Identify the blood parasite species.
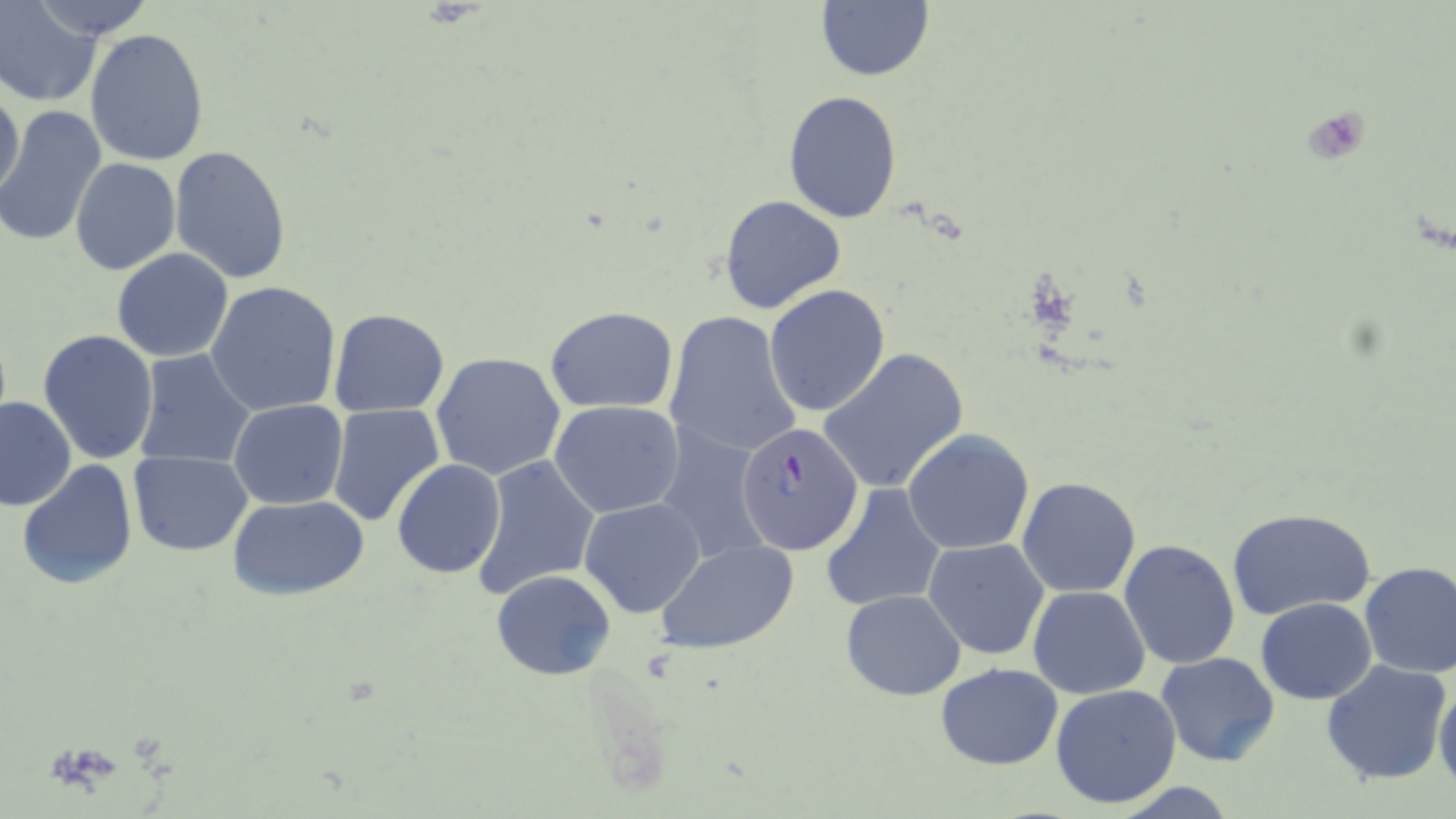
Plasmodium falciparum.

field_of_view: one of a larger specimen
modality: light microscopy
preparation: thin blood film
platelet_locations: 'approximate bounding boxes as [x1, y1, x2, y2] in pixels: [1300, 107, 1370, 165]'
magnification: 1000x
plasmodium_falciparum_infected_red_blood_cell_locations: 'approximate bounding boxes as [x1, y1, x2, y2] in pixels: [736, 422, 864, 556]'
image_size: 1456×819 pixels
stain: May-Grünwald-Giemsa
uninfected_red_blood_cell_locations: 'approximate bounding boxes as [x1, y1, x2, y2] in pixels: [0, 0, 104, 106], [24, 0, 157, 43], [814, 0, 935, 83], [84, 28, 210, 167], [0, 81, 25, 203], [783, 91, 903, 225], [1, 107, 108, 248], [169, 146, 292, 284], [70, 158, 179, 275], [720, 194, 847, 316], [112, 249, 235, 364], [206, 281, 342, 417], [765, 285, 891, 417], [544, 306, 678, 413], [327, 308, 450, 418], [664, 309, 801, 460], [37, 330, 161, 465], [817, 347, 970, 495], [132, 349, 257, 469], [431, 352, 565, 480], [0, 396, 76, 510], [228, 399, 347, 510], [550, 401, 685, 520], [326, 403, 445, 527], [656, 429, 771, 567], [903, 429, 1035, 554], [130, 452, 254, 555], [475, 456, 601, 599], [18, 459, 138, 592], [391, 459, 506, 580], [1016, 476, 1141, 600], [819, 483, 946, 614], [228, 493, 370, 600], [579, 497, 705, 617], [1227, 506, 1377, 619], [923, 538, 1051, 661], [1118, 538, 1240, 670], [655, 540, 800, 656], [1358, 560, 1456, 678], [490, 570, 618, 680], [1026, 586, 1150, 699], [840, 590, 966, 699], [1256, 598, 1376, 704], [1155, 652, 1281, 767], [1321, 659, 1453, 786], [936, 662, 1064, 771], [1433, 678, 1456, 788], [1050, 684, 1182, 809]'